Assess the morphology of the erythrocytes.
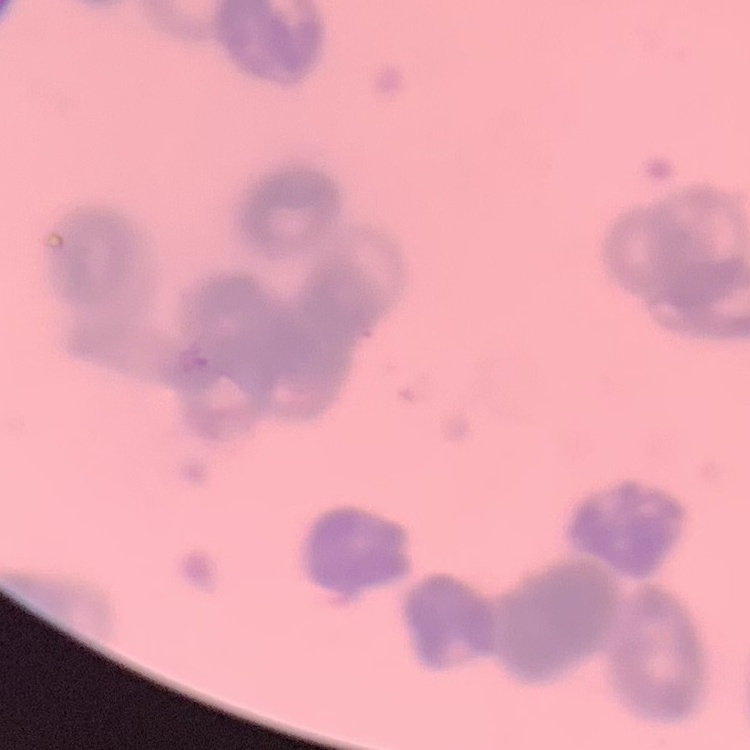
They show rouleaux formation.

Summary:
  - Image type: square crop of a larger photomicrograph
  - Preparation: thin blood smear
  - Stain: Field's or Giemsa